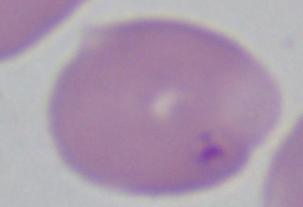
Summary:
  - Identification: Babesia
  - Magnification: 1000x
  - Modality: photomicrograph